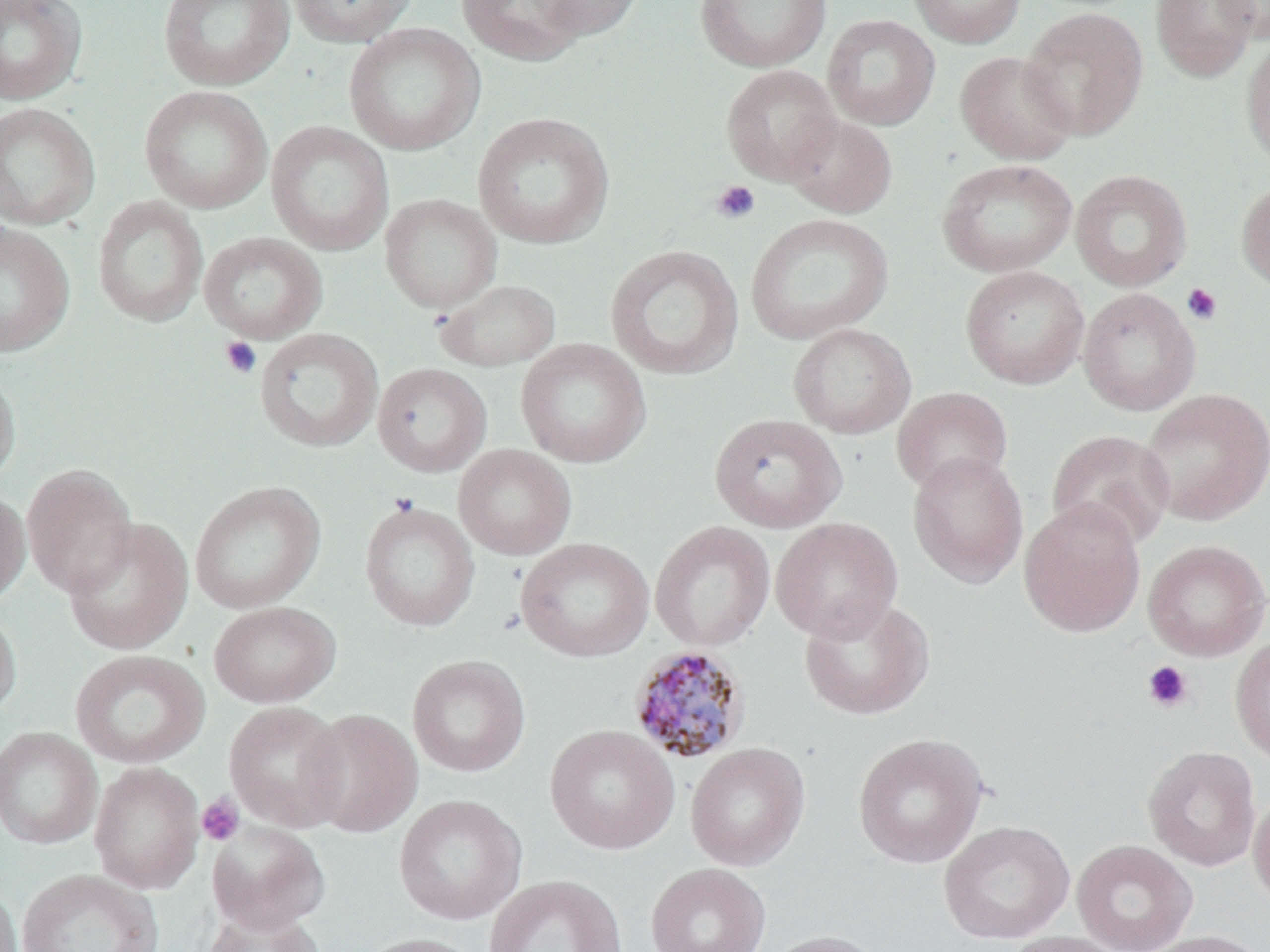

Summary:
  - Coordinate format: approximate bounding boxes as (x1, y1, x2, y2) in pixels
  - Plasmodium malariae-infected red blood cell locations: (627, 645, 752, 764)
  - Platelet locations: (710, 180, 761, 224), (1181, 283, 1223, 325), (219, 336, 262, 379), (1142, 660, 1193, 713), (197, 793, 245, 846)
  - Uninfected red blood cell locations: (157, 0, 294, 91), (286, 0, 419, 48), (456, 0, 591, 66), (527, 0, 646, 41), (694, 0, 833, 72), (907, 0, 1027, 48), (1150, 0, 1260, 82), (1213, 0, 1270, 42), (0, 1, 87, 105), (1020, 7, 1149, 140), (822, 14, 940, 130), (344, 22, 485, 156), (1240, 33, 1270, 168), (954, 51, 1077, 165), (720, 64, 841, 185), (139, 85, 273, 214), (0, 102, 101, 230), (473, 112, 615, 249), (784, 114, 898, 218), (266, 120, 393, 255), (936, 158, 1077, 277), (1070, 169, 1192, 292), (1236, 179, 1270, 292), (380, 193, 501, 312), (92, 196, 208, 326), (744, 213, 893, 345), (0, 222, 75, 357), (199, 232, 327, 344), (605, 244, 744, 381), (960, 265, 1090, 389), (436, 278, 561, 371), (1078, 288, 1200, 416), (788, 323, 916, 439), (254, 328, 384, 452), (515, 338, 651, 468), (372, 362, 493, 477), (0, 366, 21, 487), (891, 386, 1013, 496), (1138, 389, 1270, 526), (709, 413, 847, 533), (1046, 429, 1175, 550), (454, 444, 576, 559), (907, 451, 1029, 588), (21, 463, 138, 598), (189, 480, 326, 614), (0, 488, 31, 605), (1019, 498, 1146, 637), (359, 500, 480, 631), (63, 517, 193, 655), (771, 517, 903, 642), (650, 520, 775, 651), (516, 537, 654, 662), (1142, 539, 1270, 661), (799, 596, 935, 720), (208, 600, 341, 708), (0, 603, 21, 721), (1230, 634, 1270, 767), (70, 649, 209, 769), (407, 655, 531, 777), (223, 701, 350, 832), (300, 708, 422, 838), (545, 724, 680, 855), (0, 726, 102, 849), (853, 732, 988, 868), (685, 742, 810, 871), (1142, 745, 1261, 871), (89, 762, 205, 894), (1249, 791, 1270, 910), (393, 794, 527, 925), (938, 820, 1074, 944), (207, 822, 330, 934), (1071, 839, 1197, 952), (646, 862, 771, 952), (16, 868, 163, 952), (482, 874, 627, 952), (0, 882, 22, 952), (200, 904, 324, 952), (761, 929, 891, 952), (1140, 929, 1270, 952), (1000, 931, 1131, 952), (356, 932, 488, 952)
  - Slide-level diagnosis: Plasmodium malariae
  - Image size: 1270×952 pixels
  - Magnification: 1000x
  - Stain: May-Grünwald-Giemsa
  - Modality: light microscopy
  - Preparation: thin blood film
  - Field of view: one of a larger specimen